Locate every cell, classifying each as a parasitized RBC, an uninfected RBC, or a WBC.
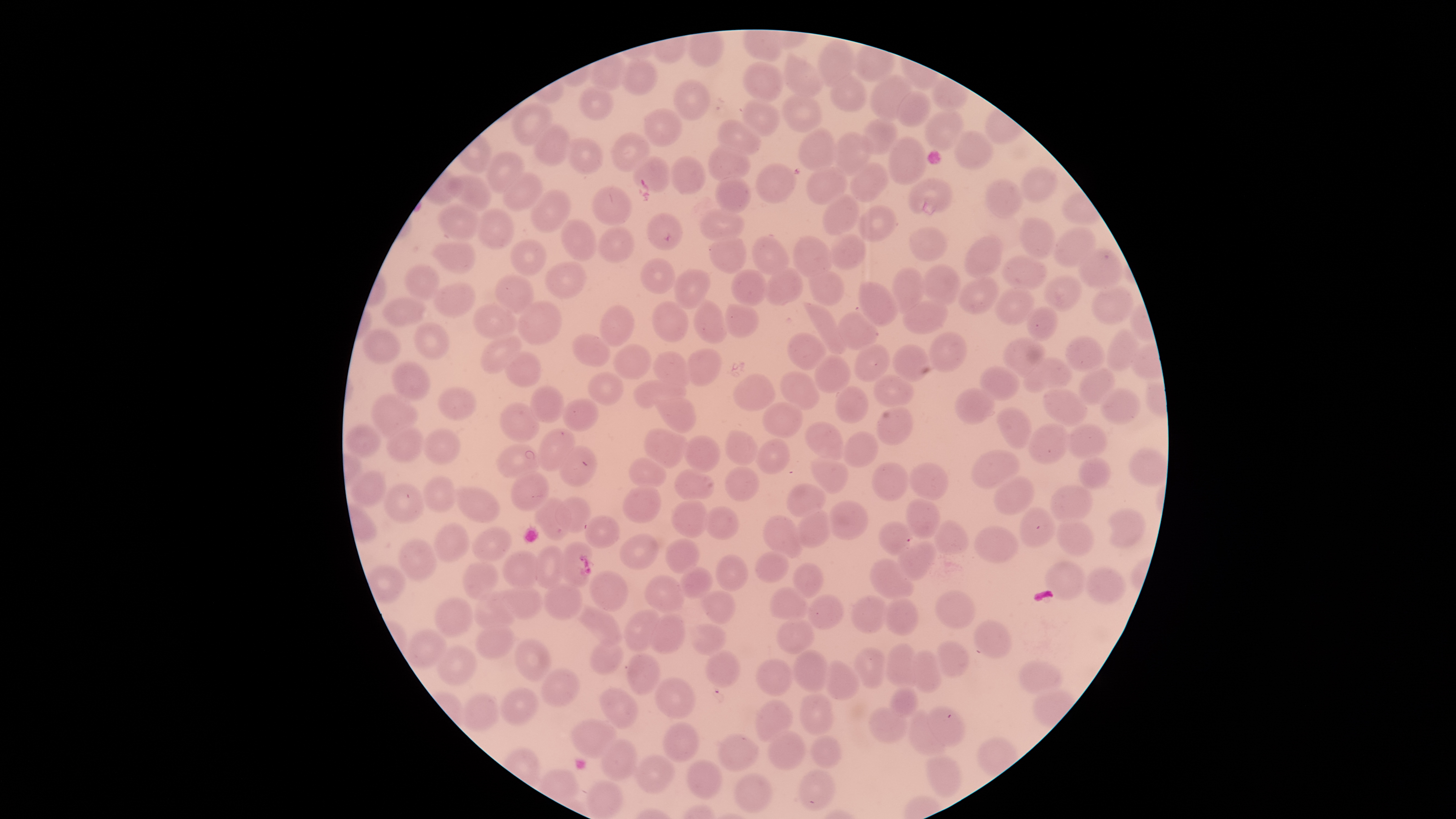
No parasitized RBCs identified.
Approximate bounding boxes as (left, top, right, bottom) in pixels.
Uninfected RBCs: (819, 40, 854, 88), (784, 59, 824, 97), (620, 60, 657, 95), (744, 62, 783, 102), (871, 75, 913, 120), (831, 76, 866, 112), (674, 80, 709, 121), (580, 88, 613, 120), (897, 92, 931, 128), (782, 93, 820, 133), (742, 99, 779, 136), (513, 104, 554, 146), (645, 109, 682, 147), (926, 110, 963, 151), (862, 119, 896, 155), (718, 120, 761, 155), (535, 124, 570, 165), (799, 127, 834, 173), (830, 132, 873, 176), (955, 132, 992, 170), (613, 133, 649, 172), (889, 137, 926, 185), (565, 138, 603, 174), (708, 146, 751, 181), (486, 153, 525, 194), (633, 157, 671, 193), (671, 157, 705, 195), (756, 162, 795, 203), (851, 162, 888, 202), (807, 166, 847, 205), (1021, 167, 1057, 203), (504, 173, 542, 211), (453, 175, 491, 212), (716, 177, 750, 213), (908, 178, 952, 216), (986, 178, 1022, 217), (592, 185, 632, 227), (532, 189, 571, 233), (822, 196, 858, 235), (437, 203, 479, 240), (859, 206, 895, 242), (701, 208, 743, 243), (476, 209, 514, 250), (647, 212, 683, 251), (561, 218, 596, 262), (1020, 219, 1055, 259), (910, 226, 947, 261), (599, 227, 634, 263), (1053, 227, 1096, 267), (709, 233, 745, 274), (829, 233, 865, 270), (965, 235, 1003, 280), (752, 236, 788, 276), (793, 236, 834, 278), (510, 238, 547, 276), (437, 243, 475, 273), (1079, 249, 1121, 291), (1002, 255, 1046, 291), (641, 258, 675, 295), (545, 261, 586, 300), (406, 264, 439, 299), (892, 266, 924, 315), (922, 266, 959, 304), (764, 267, 802, 305), (673, 269, 711, 309), (809, 269, 845, 305), (731, 270, 768, 306), (496, 274, 533, 315), (959, 276, 998, 315), (1045, 276, 1081, 311), (434, 282, 476, 318), (857, 282, 898, 327), (1092, 285, 1132, 325), (995, 286, 1034, 326), (383, 296, 425, 326), (694, 300, 725, 344), (904, 300, 949, 335), (517, 301, 561, 346), (651, 302, 688, 342), (723, 302, 758, 338), (473, 304, 516, 340), (807, 304, 846, 354), (599, 305, 635, 346), (1027, 306, 1059, 340), (838, 310, 878, 351), (414, 322, 450, 361), (362, 328, 400, 364), (1106, 329, 1140, 372), (930, 332, 967, 373), (480, 333, 521, 375), (572, 333, 609, 367), (788, 333, 827, 371), (1066, 336, 1104, 370), (1004, 337, 1046, 379), (613, 344, 651, 379), (854, 344, 891, 383), (893, 344, 928, 381), (685, 348, 721, 386), (505, 350, 541, 388), (653, 352, 691, 389), (814, 357, 849, 393), (1024, 357, 1071, 392), (392, 362, 430, 399), (981, 366, 1018, 400), (1078, 368, 1116, 405), (589, 372, 623, 406), (780, 372, 816, 407), (734, 374, 774, 412), (872, 374, 913, 409), (633, 379, 685, 408), (835, 385, 868, 423), (529, 386, 566, 423), (1043, 386, 1087, 426), (438, 387, 476, 420), (956, 387, 994, 424), (1100, 389, 1140, 424), (658, 396, 695, 433), (371, 397, 417, 438), (562, 398, 598, 431), (499, 402, 540, 443), (760, 403, 802, 437), (877, 406, 912, 446), (997, 407, 1033, 448), (805, 422, 842, 458), (1029, 424, 1068, 463), (1065, 424, 1106, 459), (344, 426, 380, 457), (386, 426, 423, 464), (536, 428, 573, 472), (645, 428, 688, 469), (422, 429, 460, 465), (723, 431, 760, 465), (844, 431, 878, 468), (682, 436, 720, 474), (757, 439, 789, 474), (496, 444, 537, 478), (558, 447, 597, 487), (1129, 448, 1166, 486), (970, 450, 1021, 489), (1079, 455, 1110, 489), (811, 457, 847, 493), (629, 459, 666, 489), (870, 462, 909, 500), (908, 463, 950, 501), (673, 467, 714, 504), (724, 467, 758, 501), (352, 471, 387, 506), (509, 471, 550, 511), (993, 475, 1036, 516), (420, 476, 456, 513), (384, 482, 424, 523), (623, 484, 662, 523), (787, 484, 826, 517), (456, 486, 500, 524), (1050, 486, 1091, 522), (535, 497, 571, 541), (556, 497, 591, 531), (904, 498, 940, 539), (671, 499, 707, 537), (826, 500, 869, 541), (704, 505, 738, 540), (1019, 507, 1057, 548), (1105, 509, 1145, 546), (795, 511, 831, 547), (584, 515, 619, 550), (764, 515, 801, 558), (932, 519, 970, 555), (1057, 519, 1095, 557), (878, 521, 915, 557), (433, 522, 469, 562), (973, 525, 1020, 563), (473, 527, 511, 562), (619, 533, 659, 569), (666, 539, 699, 574), (398, 540, 436, 580), (559, 542, 593, 587), (896, 542, 937, 581), (536, 545, 564, 590), (503, 550, 541, 591), (756, 550, 789, 583), (716, 554, 748, 591), (869, 558, 915, 600), (462, 561, 498, 599), (1045, 561, 1084, 601), (792, 563, 825, 597), (680, 566, 711, 599), (1085, 566, 1123, 604), (589, 571, 627, 612), (645, 575, 684, 613), (544, 583, 581, 621), (507, 586, 542, 620), (771, 586, 806, 624), (701, 590, 737, 623), (934, 590, 976, 629), (472, 592, 514, 632), (807, 594, 843, 630), (851, 595, 889, 634), (435, 596, 474, 638), (882, 599, 921, 635), (574, 605, 623, 645), (624, 608, 661, 653), (650, 613, 685, 654), (777, 617, 814, 654), (973, 619, 1013, 659), (476, 623, 514, 659), (691, 624, 727, 655), (408, 628, 446, 668), (514, 640, 552, 682), (589, 640, 624, 675), (935, 641, 971, 677), (884, 643, 920, 687), (436, 646, 478, 685), (856, 647, 886, 690), (794, 650, 829, 692), (705, 651, 741, 688), (909, 651, 943, 692), (627, 653, 659, 695), (756, 658, 793, 696), (824, 660, 859, 700), (1018, 660, 1063, 695), (542, 668, 579, 707), (656, 677, 695, 720), (500, 687, 538, 725), (599, 687, 639, 728), (889, 687, 920, 717), (799, 694, 833, 737), (464, 695, 498, 730), (754, 700, 793, 743), (928, 706, 963, 746), (867, 707, 908, 744), (907, 713, 948, 758), (571, 720, 618, 760), (661, 722, 700, 762), (767, 731, 806, 771), (719, 733, 759, 772), (811, 734, 843, 769), (601, 739, 638, 780), (634, 754, 674, 793), (925, 755, 963, 799), (685, 759, 722, 800), (799, 769, 834, 812), (733, 773, 773, 812), (587, 780, 622, 817).
No WBCs identified.

{
  "stain": "Giemsa",
  "preparation": "thin smear of blood",
  "field_of_view": "single",
  "visible_region": "circular",
  "capture": "smartphone photograph through the microscope eyepiece",
  "image_size": "1456×819 pixels"
}